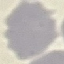
Summary:
  - Malaria status: uninfected
  - Preparation: thin blood smear
  - Capture: smartphone through the microscope eyepiece
  - Stain: Giemsa
  - Image type: automatically extracted cell patch, resized to 64 × 64 pixels